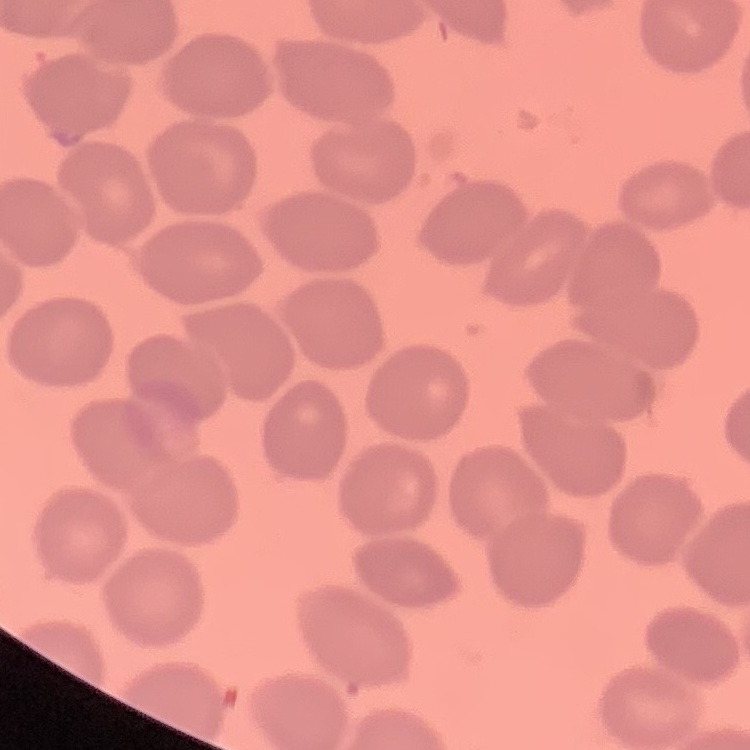

{
  "erythrocyte_morphology": "no rouleaux formation",
  "image_type": "one tile cut from a larger photomicrograph",
  "stain": "Field's or Giemsa",
  "preparation": "thin blood smear"
}